Comment on the morphology of the erythrocytes.
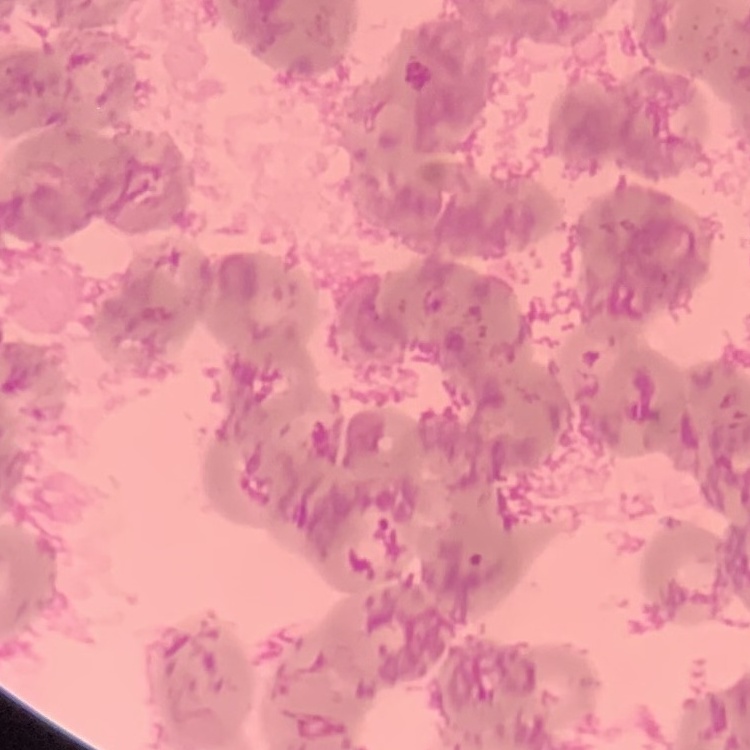
Rouleaux formation.

One tile cut from a larger photomicrograph. Field's or Giemsa stain. Thin peripheral smear.